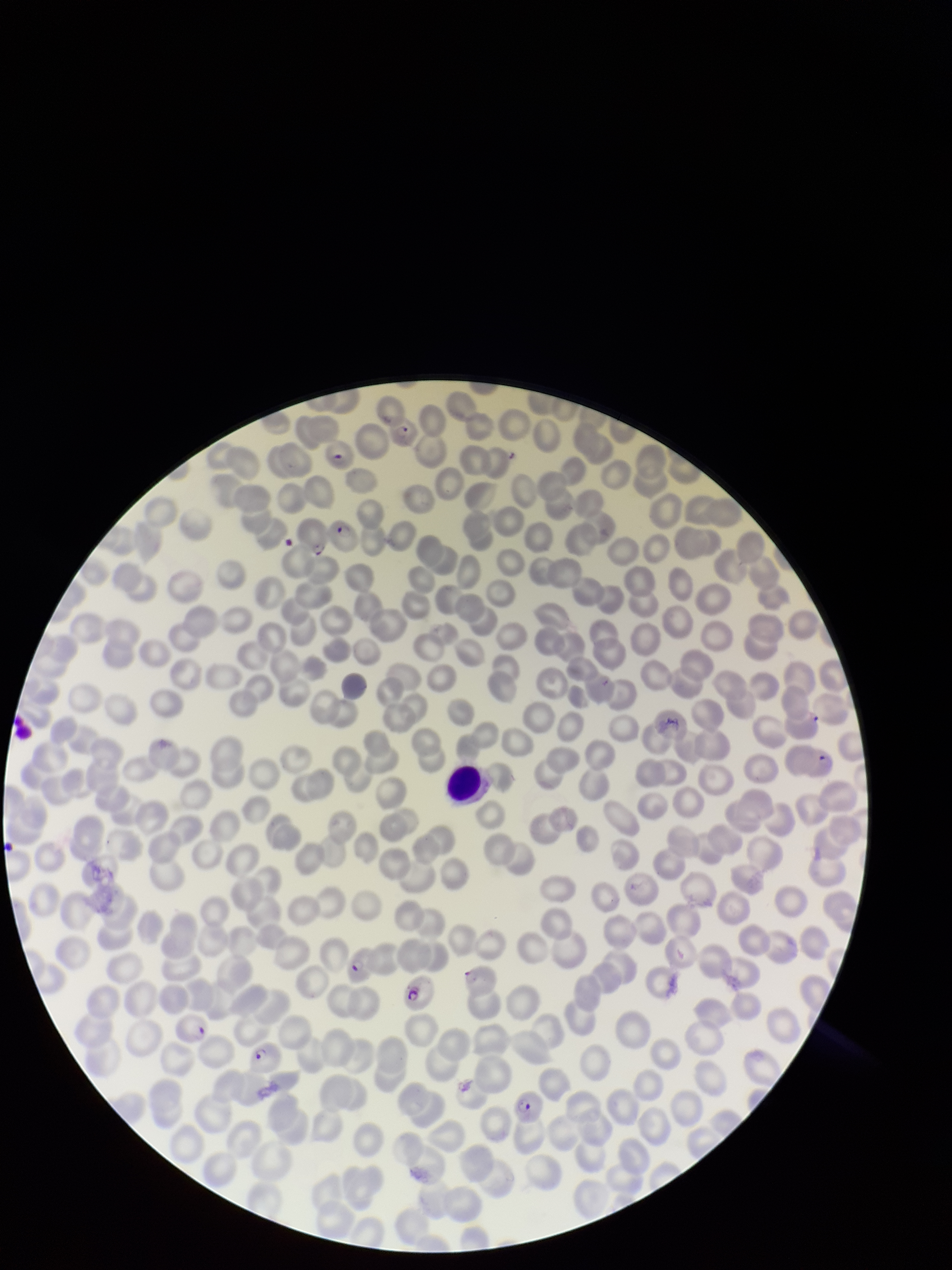
Patient malaria status: positive. Image is 952×1270 pixels. Red blood cell count: 229. Parasitized red blood cells: identified. Single field of view. Stained with Giemsa. Species reported for this patient: Plasmodium falciparum. Preparation: thin. Parasitized red blood cell count: 11. Photographed through the microscope eyepiece with a smartphone camera.